Report the malaria status of this cell.
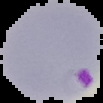
It is parasitized.

Image is 103×103 pixels. Segmented cell region on a black background. From a thin blood smear.